Identify the parasite.
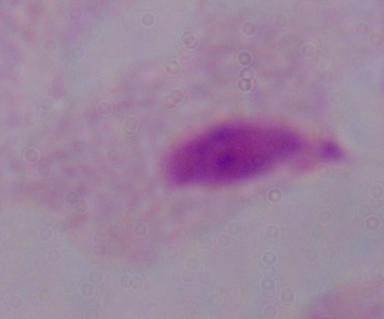
A trichomonad.

modality = photomicrograph
magnification = 1000x